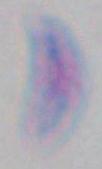 Captured at 1000x magnification. Toxoplasma gondii is shown. Micrograph.